Identify the parasite.
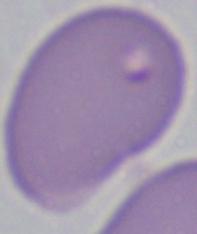

Babesia.

Summary:
  - Magnification: 1000x
  - Modality: micrograph